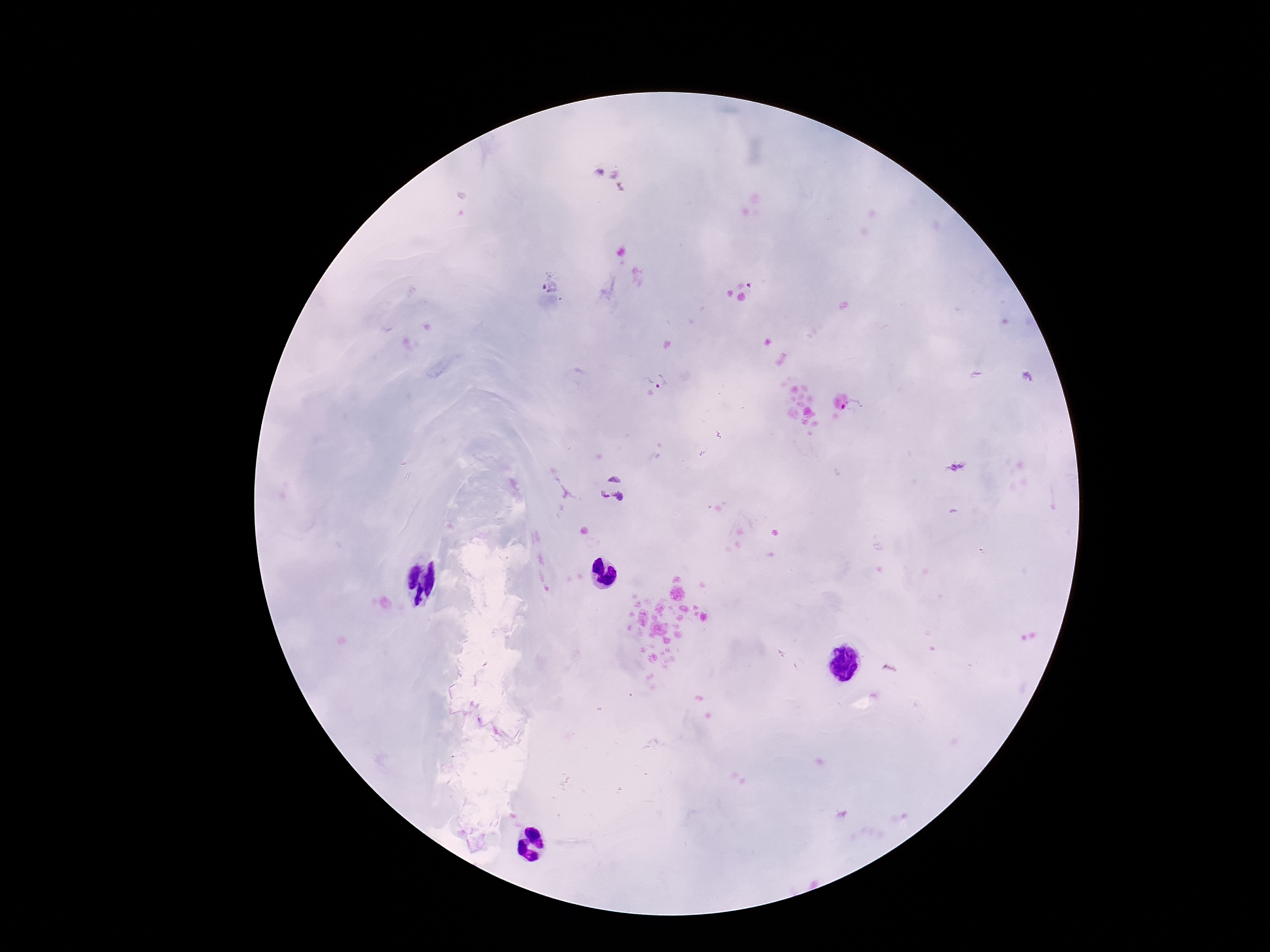

Approximate object centers, in pixels from the top-left corner.
Summary:
  - Plasmodium parasite locations: (x=550, y=284), (x=657, y=381), (x=956, y=466), (x=613, y=487)
  - Image size: 1270×952 pixels
  - Field of view: one from this slide
  - Magnification: 100x
  - Patient malaria status: infected
  - Stain: Giemsa
  - Preparation: thick blood film
  - Capture: smartphone camera through the microscope eyepiece